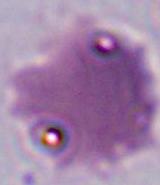
{
  "magnification": "400x or 1000x",
  "modality": "photomicrograph",
  "identification": "Plasmodium"
}